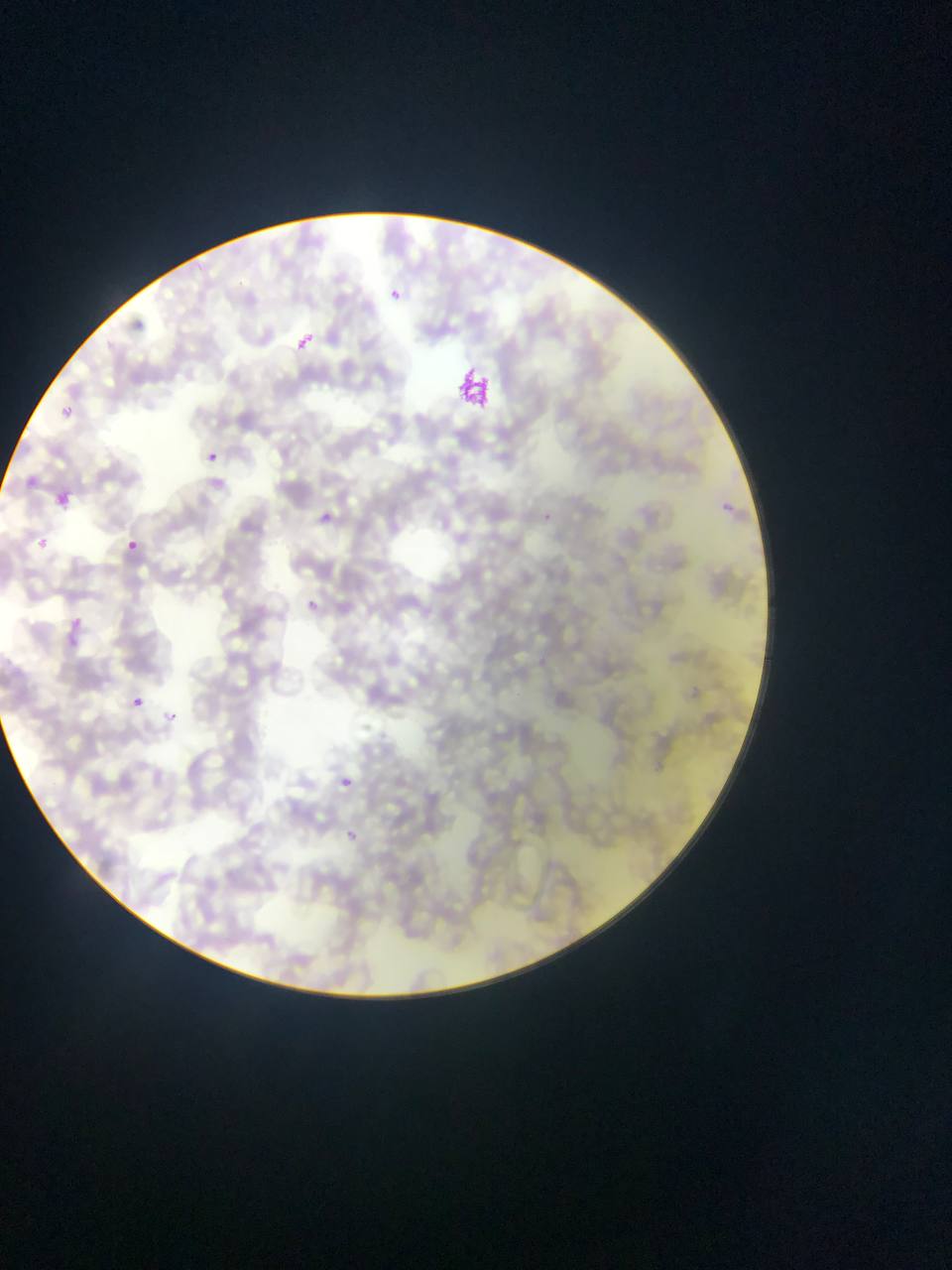
Approximate bounding boxes as [left, top, right, bottom] in pixels.
Summary:
  - Plasmodium parasite locations: [390, 282, 409, 304], [284, 325, 326, 348], [56, 403, 91, 433], [207, 450, 219, 461], [19, 464, 45, 483], [57, 494, 69, 506], [724, 497, 746, 529], [542, 508, 561, 533], [319, 510, 344, 533], [38, 538, 49, 549], [128, 539, 139, 549], [307, 600, 318, 610], [69, 613, 82, 627], [61, 625, 89, 654], [132, 696, 143, 708], [163, 706, 192, 726], [339, 774, 354, 793], [338, 825, 358, 849]
  - Artifact (stain precipitate or debris) locations: [456, 366, 499, 413]
  - Country: Ghana
  - Image size: 952×1270 pixels
  - Capture: mobile-phone photograph through a microscope
  - Field of view: single
  - Preparation: thin blood smear